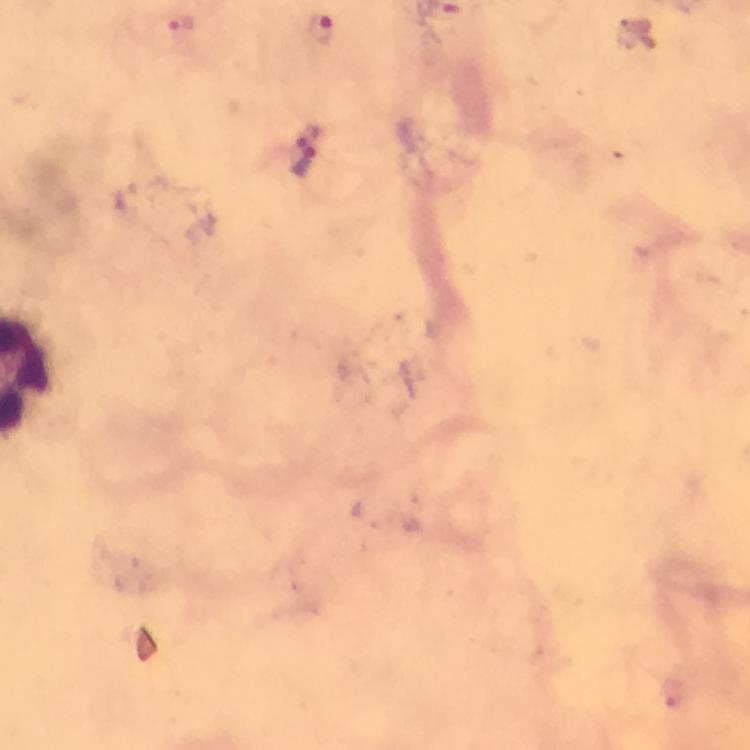
Approximate centers as [x, y] in pixels. Plasmodium parasite locations: [178, 22], [319, 28], [313, 134], [304, 166], [668, 691]. Image is 750×750 pixels. Photographed through the microscope with a smartphone camera. Immersion oil was used. Thick blood film. Giemsa stain. At 100x magnification. Cropped region of a single field of view. From a diagnostic examination for malaria.